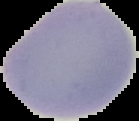
From a thin blood film. Segmented cell region on a black background. Image is 139×121 pixels. Result: negative for Plasmodium parasites.